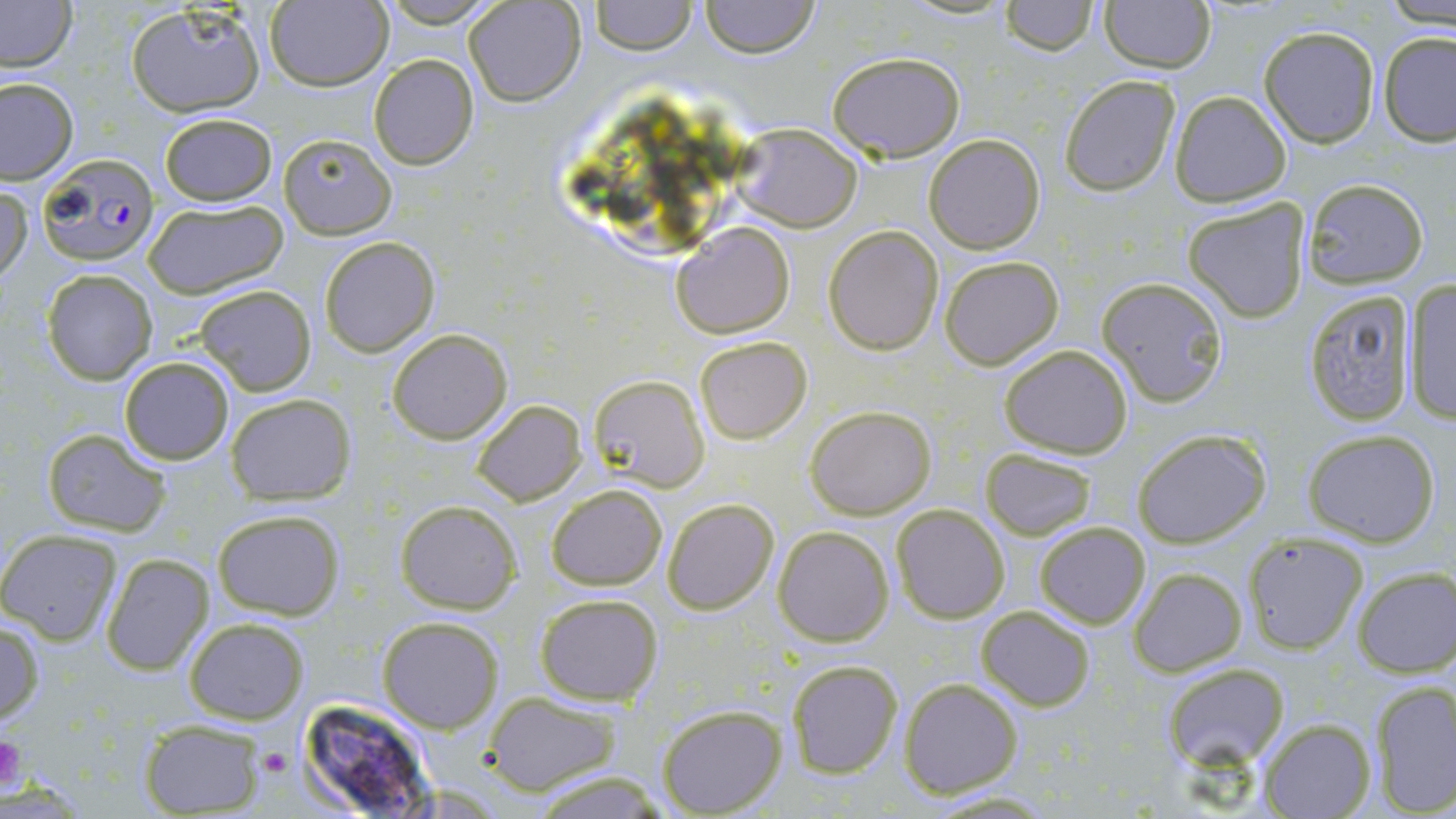
Plasmodium falciparum-infected red blood cell locations = approximate bounding boxes as (x1, y1, x2, y2) in pixels: (35, 153, 160, 268)
slide-level diagnosis = Plasmodium falciparum
preparation = thin blood film
magnification = 1000x
image size = 1456×819 pixels
stain = May-Grünwald-Giemsa
uninfected red blood cell locations = approximate bounding boxes as (x1, y1, x2, y2) in pixels: (377, 0, 502, 26), (465, 0, 585, 106), (590, 0, 695, 53), (700, 0, 820, 58), (0, 1, 77, 73), (265, 1, 391, 89), (1001, 1, 1098, 54), (1099, 1, 1217, 73), (1382, 1, 1455, 28), (125, 3, 266, 118), (1259, 25, 1380, 148), (1378, 31, 1456, 145), (827, 51, 965, 161), (368, 55, 479, 170), (1060, 75, 1180, 194), (1, 77, 78, 184), (1168, 92, 1292, 207), (158, 112, 279, 206), (731, 124, 863, 233), (278, 133, 396, 238), (924, 133, 1046, 254), (1302, 178, 1430, 287), (1, 185, 31, 288), (1182, 198, 1311, 324), (144, 199, 288, 298), (671, 223, 795, 337), (823, 226, 943, 356), (319, 238, 439, 356), (939, 255, 1065, 371), (41, 269, 157, 385), (1096, 276, 1230, 408), (1402, 279, 1455, 423), (195, 283, 317, 395), (1301, 289, 1418, 425), (386, 328, 511, 444), (695, 336, 812, 443), (998, 345, 1132, 458), (119, 355, 235, 465), (587, 374, 709, 492), (226, 393, 355, 503), (473, 399, 588, 506), (805, 405, 936, 519), (41, 428, 171, 537), (1132, 428, 1272, 549), (1301, 429, 1442, 546), (980, 448, 1099, 540), (546, 484, 667, 589), (662, 498, 779, 616), (395, 500, 520, 613), (891, 503, 1009, 623), (211, 508, 345, 620), (1034, 521, 1150, 629), (772, 526, 893, 646), (1243, 530, 1368, 654), (1, 531, 122, 645), (102, 554, 213, 676), (1352, 566, 1456, 676), (1130, 567, 1245, 676), (536, 593, 664, 706), (976, 605, 1094, 711), (378, 616, 502, 732), (0, 618, 45, 724), (184, 618, 309, 724), (786, 660, 903, 777), (1163, 663, 1287, 765), (900, 678, 1022, 797), (1369, 680, 1456, 816), (482, 692, 624, 795), (657, 704, 786, 816), (1259, 717, 1376, 818), (140, 718, 267, 816), (525, 768, 671, 818)
field of view = one of a larger specimen
modality = optical microscopy
platelet locations = approximate bounding boxes as (x1, y1, x2, y2) in pixels: (0, 733, 25, 794), (260, 745, 293, 775)